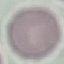
result = no malaria parasites detected
preparation = thin smear
image type = cell patch, automatically extracted from a larger field of view and resized to 64 × 64 pixels
capture = smartphone through the microscope eyepiece
stain = Giemsa